Assess this cell for malaria.
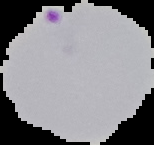

It is parasitized.

image_size: 154×145 pixels
preparation: thin blood film
image_type: segmented cell region on a black background